Assess this cell for malaria.
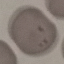

It is uninfected.

capture: smartphone through the microscope eyepiece
image_type: cell patch, automatically extracted from a larger field of view and resized to 64 × 64 pixels
preparation: thin blood film
stain: Giemsa